Locate and identify every blood parasite.
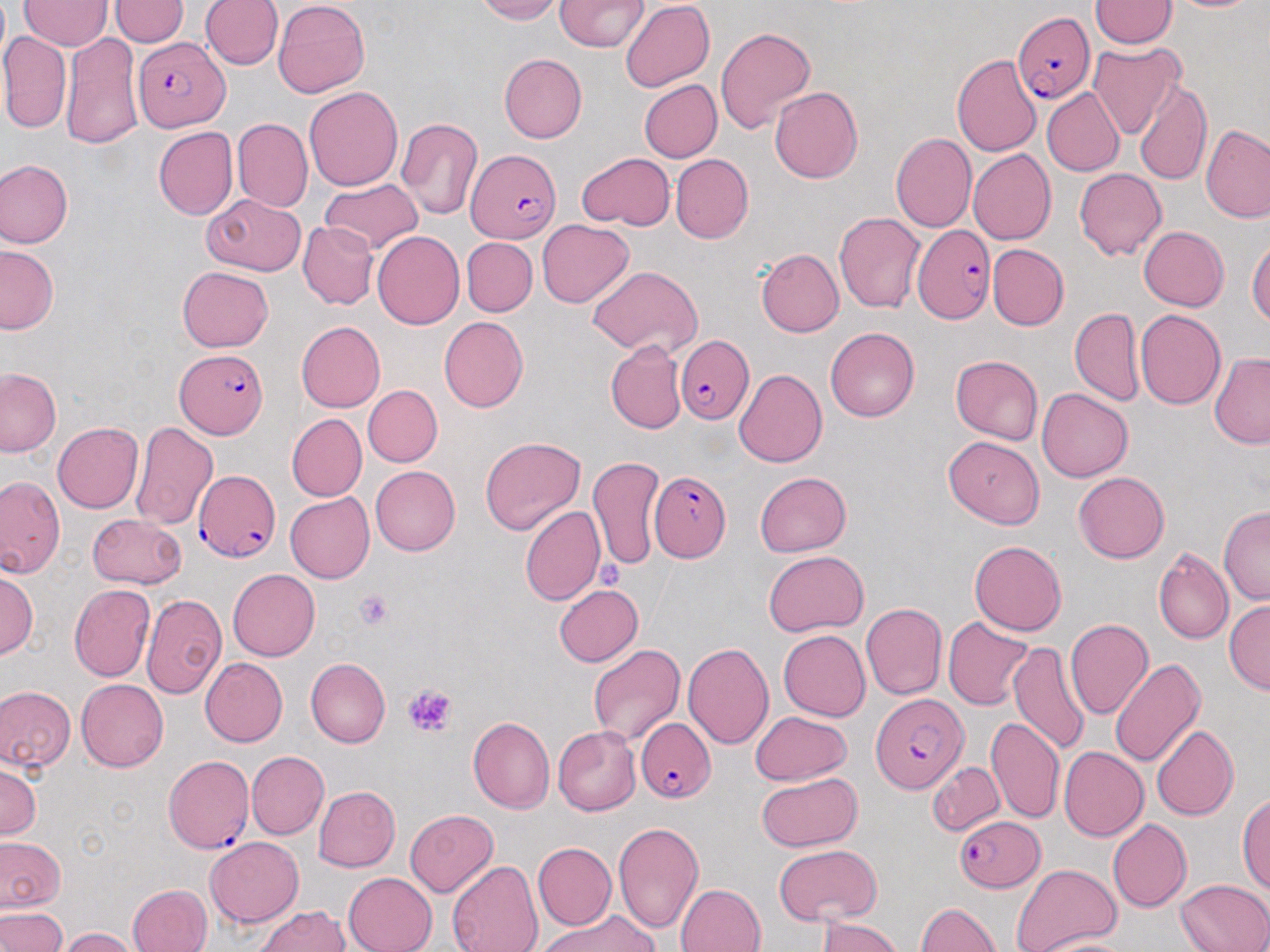
Approximate bounding boxes as (x1,y1)-(x2,y2) corner pairs in pixels.
Plasmodium falciparum-infected red blood cells: (1014,12)-(1094,103), (132,37)-(231,131), (465,150)-(560,243), (913,225)-(996,322), (677,336)-(751,422), (174,350)-(270,437), (195,470)-(279,562), (650,472)-(730,560), (872,694)-(967,793), (637,717)-(715,803), (165,756)-(254,857), (954,815)-(1045,893).
No Plasmodium ovale, Plasmodium malariae, Plasmodium vivax, Babesia divergens, or Trypanosoma brucei observed.

{
  "slide_level_diagnosis": "Plasmodium falciparum",
  "platelet_locations": "approximate bounding boxes as (x1,y1)-(x2,y2) corner pairs in pixels: (353,589)-(394,630), (403,682)-(459,737)",
  "image_size": "1270×952 pixels",
  "modality": "light microscopy",
  "uninfected_red_blood_cell_locations": "approximate bounding boxes as (x1,y1)-(x2,y2) corner pairs in pixels: (109,0)-(188,46), (201,0)-(283,69), (274,0)-(368,98), (471,0)-(562,23), (554,0)-(648,51), (1088,0)-(1178,48), (20,1)-(113,50), (620,1)-(714,92), (715,26)-(816,134), (0,32)-(72,134), (62,32)-(143,149), (1088,43)-(1186,140), (499,53)-(587,144), (953,53)-(1041,156), (639,79)-(721,163), (1135,79)-(1211,186), (769,86)-(863,183), (305,87)-(403,190), (1041,87)-(1124,176), (396,116)-(484,220), (233,117)-(313,212), (1202,123)-(1270,222), (153,126)-(237,219), (890,133)-(976,232), (968,148)-(1056,244), (577,153)-(675,229), (670,154)-(753,243), (0,160)-(73,247), (1075,168)-(1167,260), (320,177)-(423,255), (202,193)-(306,277), (834,211)-(925,314), (537,219)-(634,307), (298,221)-(379,309), (1139,226)-(1228,311), (372,231)-(465,329), (1248,235)-(1270,327), (462,237)-(537,317), (0,244)-(59,335), (987,244)-(1069,330), (756,247)-(844,337), (588,265)-(703,357), (178,267)-(273,352), (1069,307)-(1144,405), (1135,309)-(1226,409), (438,316)-(527,413), (296,320)-(385,412), (825,328)-(920,422), (605,340)-(686,434), (1209,353)-(1270,449), (950,355)-(1043,446), (0,368)-(60,457), (734,368)-(827,467), (362,385)-(442,467), (1037,388)-(1133,482), (287,413)-(367,501), (130,420)-(218,530), (53,423)-(144,513), (480,436)-(586,536), (943,436)-(1045,527), (587,456)-(664,572), (370,465)-(460,556), (754,470)-(851,557), (1073,471)-(1169,562), (0,476)-(64,579), (285,493)-(375,583), (1219,505)-(1270,605), (519,506)-(604,607), (87,513)-(188,588), (969,540)-(1066,636), (1153,547)-(1234,645), (763,550)-(869,636), (0,568)-(36,659), (228,569)-(319,661), (69,584)-(154,682), (554,586)-(643,666), (141,593)-(227,700), (1223,600)-(1270,694), (860,603)-(947,700), (942,616)-(1035,709), (1065,619)-(1154,720), (778,631)-(870,721), (1034,631)-(1136,745), (1008,642)-(1091,755), (683,643)-(774,749), (587,644)-(685,747), (305,657)-(390,748), (201,658)-(287,747), (1110,659)-(1206,768), (76,679)-(168,771), (1,686)-(76,773), (749,712)-(852,786), (468,715)-(555,813), (986,716)-(1065,825), (553,725)-(641,816), (1152,725)-(1239,821), (1059,746)-(1149,842), (247,751)-(328,840), (0,761)-(40,840), (927,761)-(1005,836), (756,773)-(861,852), (313,785)-(400,872), (1237,792)-(1270,894), (405,809)-(499,896), (1107,818)-(1191,912), (612,821)-(704,934), (0,836)-(65,912), (205,837)-(303,927), (533,842)-(616,929), (773,845)-(881,927), (447,859)-(543,952), (1012,863)-(1121,952), (343,872)-(437,952), (1175,879)-(1270,952), (127,883)-(211,952), (676,883)-(766,952), (916,902)-(1000,952), (254,905)-(351,952), (0,907)-(68,952), (537,911)-(658,952), (817,916)-(900,952), (58,927)-(140,952), (1030,936)-(1140,952)",
  "preparation": "thin blood smear",
  "magnification": "1000x",
  "field_of_view": "single",
  "stain": "May-Grünwald-Giemsa"
}